Assess for Plasmodium parasites.
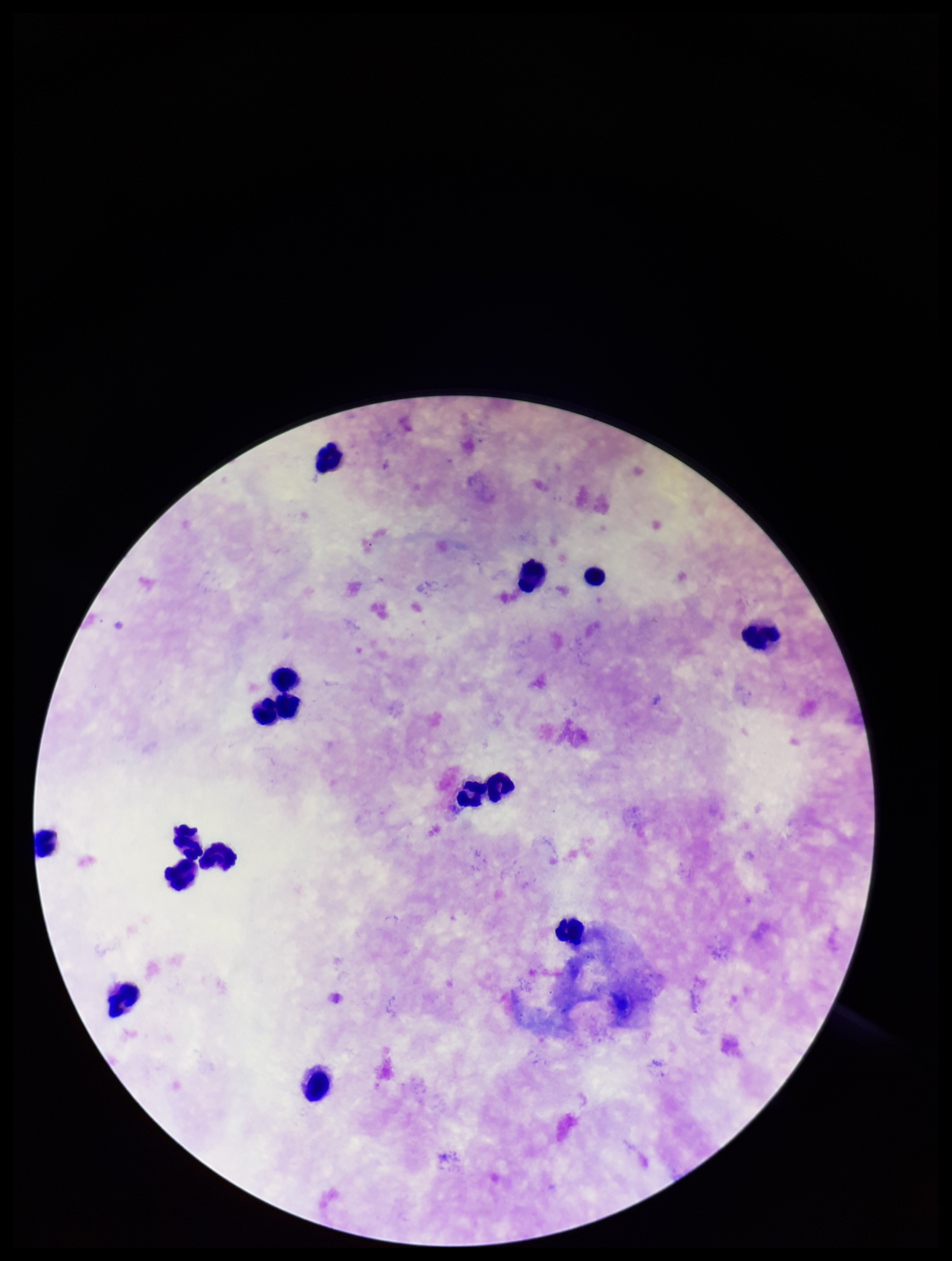
None seen.

Summary:
  - Parasite count: 0
  - Field of view: one from this slide
  - Species reported for this patient: Plasmodium falciparum
  - Leukocyte count: 16
  - Patient malaria status: positive
  - Capture: smartphone photograph through the microscope eyepiece
  - Image size: 952×1261 pixels
  - Preparation: thick blood smear
  - Stain: Giemsa